Assess this cell for malaria.
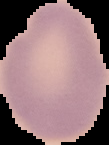
Uninfected.

Summary:
  - Image size: 109×145 pixels
  - Preparation: thin blood film
  - Image type: segmented cell region with the area outside set to black